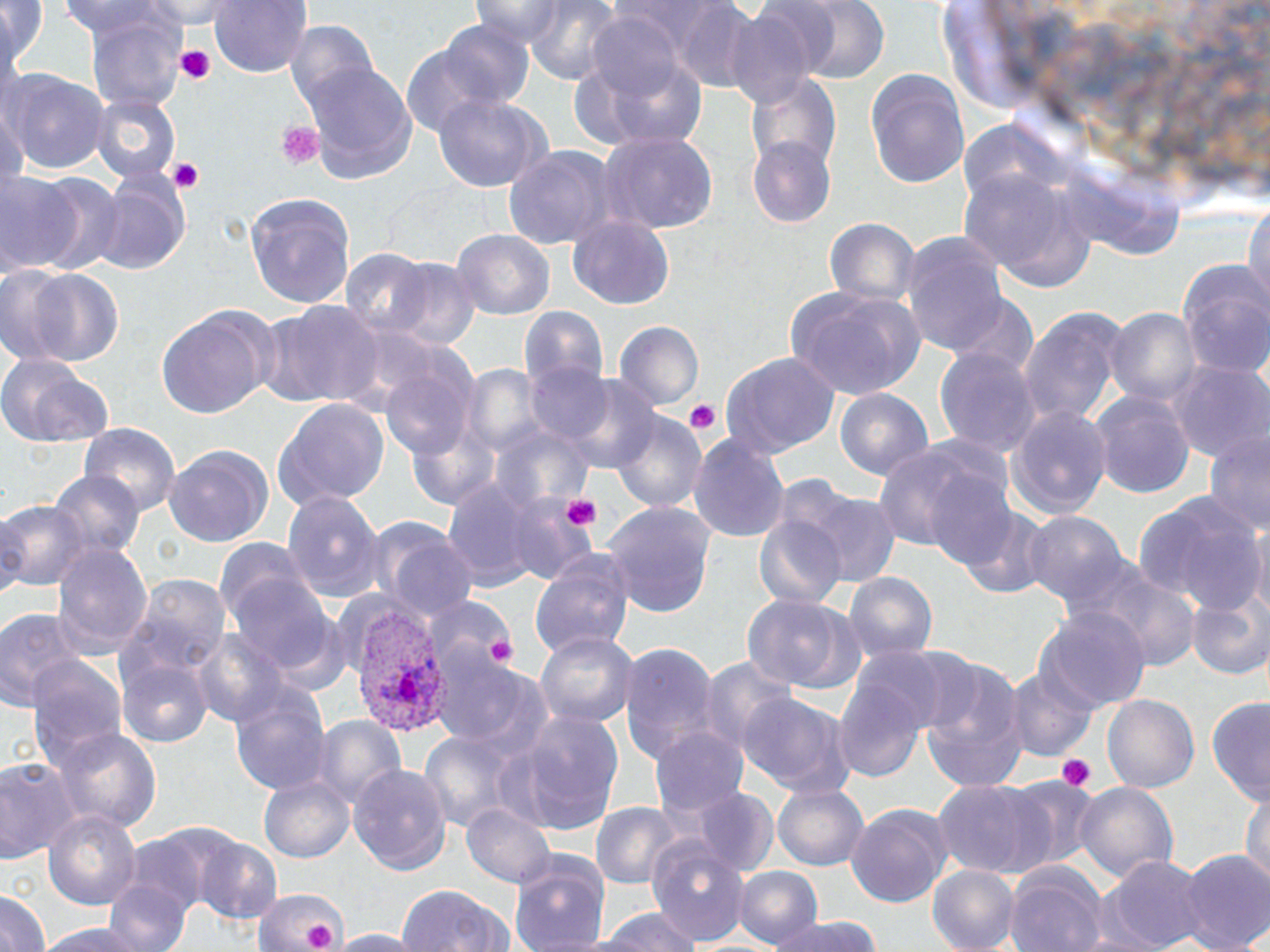 Approximate bounding boxes as named x1/y1/x2/y2 corners in pixels. Uninfected red blood cell locations: (x1=0, y1=0, x2=47, y2=87), (x1=144, y1=0, x2=250, y2=29), (x1=209, y1=0, x2=311, y2=80), (x1=469, y1=0, x2=575, y2=42), (x1=521, y1=0, x2=627, y2=86), (x1=789, y1=0, x2=890, y2=84), (x1=53, y1=2, x2=185, y2=42), (x1=664, y1=2, x2=762, y2=89), (x1=81, y1=7, x2=192, y2=116), (x1=721, y1=7, x2=821, y2=112), (x1=583, y1=10, x2=691, y2=104), (x1=432, y1=17, x2=536, y2=111), (x1=286, y1=22, x2=383, y2=123), (x1=400, y1=42, x2=504, y2=139), (x1=570, y1=47, x2=710, y2=158), (x1=299, y1=60, x2=417, y2=182), (x1=864, y1=67, x2=970, y2=189), (x1=4, y1=71, x2=109, y2=178), (x1=745, y1=71, x2=841, y2=174), (x1=92, y1=94, x2=180, y2=184), (x1=432, y1=94, x2=550, y2=193), (x1=599, y1=132, x2=717, y2=236), (x1=747, y1=137, x2=837, y2=229), (x1=502, y1=144, x2=622, y2=249), (x1=954, y1=167, x2=1094, y2=287), (x1=93, y1=170, x2=192, y2=274), (x1=24, y1=171, x2=122, y2=277), (x1=0, y1=175, x2=82, y2=272), (x1=246, y1=194, x2=355, y2=308), (x1=1243, y1=201, x2=1270, y2=320), (x1=568, y1=214, x2=676, y2=312), (x1=825, y1=218, x2=920, y2=309), (x1=451, y1=231, x2=554, y2=321), (x1=899, y1=234, x2=1012, y2=360), (x1=337, y1=248, x2=439, y2=343), (x1=1176, y1=258, x2=1270, y2=379), (x1=389, y1=262, x2=480, y2=354), (x1=19, y1=267, x2=124, y2=369), (x1=784, y1=286, x2=927, y2=399), (x1=946, y1=297, x2=1039, y2=382), (x1=254, y1=299, x2=381, y2=409), (x1=1017, y1=304, x2=1132, y2=429), (x1=157, y1=305, x2=273, y2=418), (x1=521, y1=306, x2=607, y2=392), (x1=1105, y1=308, x2=1200, y2=414), (x1=614, y1=321, x2=704, y2=410), (x1=934, y1=347, x2=1038, y2=456), (x1=722, y1=351, x2=840, y2=455), (x1=0, y1=354, x2=117, y2=450), (x1=383, y1=358, x2=476, y2=462), (x1=1170, y1=360, x2=1267, y2=461), (x1=524, y1=362, x2=616, y2=447), (x1=562, y1=376, x2=662, y2=477), (x1=833, y1=388, x2=934, y2=486), (x1=1090, y1=392, x2=1197, y2=499), (x1=274, y1=396, x2=391, y2=511), (x1=1006, y1=407, x2=1113, y2=519), (x1=610, y1=409, x2=705, y2=513), (x1=80, y1=422, x2=178, y2=513), (x1=689, y1=431, x2=790, y2=546), (x1=1203, y1=431, x2=1270, y2=539), (x1=875, y1=439, x2=1010, y2=561), (x1=162, y1=444, x2=272, y2=550), (x1=53, y1=471, x2=143, y2=564), (x1=927, y1=473, x2=1021, y2=570), (x1=440, y1=477, x2=552, y2=593), (x1=798, y1=488, x2=900, y2=587), (x1=282, y1=489, x2=385, y2=603), (x1=1135, y1=491, x2=1263, y2=616), (x1=503, y1=496, x2=597, y2=583), (x1=0, y1=499, x2=91, y2=599), (x1=603, y1=502, x2=715, y2=619), (x1=959, y1=507, x2=1057, y2=601), (x1=367, y1=512, x2=473, y2=621), (x1=1022, y1=512, x2=1129, y2=612), (x1=754, y1=513, x2=846, y2=611), (x1=1251, y1=518, x2=1269, y2=619), (x1=51, y1=539, x2=153, y2=659), (x1=531, y1=549, x2=637, y2=663), (x1=1066, y1=558, x2=1199, y2=670), (x1=844, y1=571, x2=938, y2=663), (x1=224, y1=573, x2=344, y2=679), (x1=120, y1=575, x2=230, y2=693), (x1=1187, y1=591, x2=1270, y2=680), (x1=426, y1=593, x2=518, y2=671), (x1=740, y1=594, x2=852, y2=695), (x1=0, y1=606, x2=83, y2=714), (x1=1040, y1=607, x2=1150, y2=711), (x1=536, y1=628, x2=638, y2=732), (x1=193, y1=629, x2=290, y2=729), (x1=618, y1=643, x2=720, y2=763), (x1=890, y1=646, x2=984, y2=735), (x1=700, y1=655, x2=796, y2=755), (x1=119, y1=657, x2=210, y2=746), (x1=26, y1=658, x2=126, y2=772), (x1=437, y1=661, x2=555, y2=758), (x1=921, y1=662, x2=1028, y2=790), (x1=1006, y1=662, x2=1099, y2=760), (x1=832, y1=672, x2=930, y2=785), (x1=230, y1=680, x2=331, y2=797), (x1=738, y1=692, x2=856, y2=796), (x1=1101, y1=695, x2=1199, y2=794), (x1=1208, y1=701, x2=1270, y2=805), (x1=507, y1=709, x2=626, y2=836), (x1=311, y1=716, x2=408, y2=811), (x1=55, y1=723, x2=162, y2=834), (x1=650, y1=725, x2=751, y2=822), (x1=417, y1=730, x2=521, y2=835), (x1=0, y1=758, x2=78, y2=866), (x1=348, y1=763, x2=452, y2=874), (x1=260, y1=773, x2=354, y2=864), (x1=1005, y1=775, x2=1105, y2=869), (x1=932, y1=780, x2=1057, y2=880), (x1=773, y1=781, x2=870, y2=870), (x1=1074, y1=781, x2=1177, y2=883), (x1=694, y1=790, x2=779, y2=880), (x1=1241, y1=791, x2=1270, y2=889), (x1=592, y1=801, x2=681, y2=893), (x1=462, y1=802, x2=558, y2=889), (x1=845, y1=804, x2=952, y2=907), (x1=43, y1=807, x2=143, y2=911), (x1=193, y1=838, x2=283, y2=925), (x1=648, y1=838, x2=753, y2=943), (x1=1181, y1=849, x2=1270, y2=952), (x1=510, y1=850, x2=612, y2=952), (x1=1105, y1=856, x2=1209, y2=950), (x1=1005, y1=864, x2=1108, y2=952), (x1=733, y1=866, x2=822, y2=948), (x1=927, y1=866, x2=1019, y2=951), (x1=105, y1=879, x2=195, y2=952), (x1=395, y1=884, x2=515, y2=952), (x1=253, y1=886, x2=347, y2=952), (x1=0, y1=892, x2=52, y2=952), (x1=590, y1=906, x2=703, y2=952), (x1=772, y1=915, x2=884, y2=952), (x1=35, y1=918, x2=166, y2=952), (x1=323, y1=930, x2=423, y2=951). Plasmodium vivax-infected red blood cell locations: (x1=342, y1=608, x2=449, y2=735). Platelet locations: (x1=175, y1=45, x2=217, y2=87), (x1=276, y1=120, x2=325, y2=170), (x1=167, y1=158, x2=205, y2=192), (x1=683, y1=399, x2=721, y2=435), (x1=559, y1=494, x2=603, y2=531), (x1=487, y1=634, x2=515, y2=666), (x1=1056, y1=756, x2=1095, y2=790), (x1=303, y1=920, x2=334, y2=948). Slide-level diagnosis: Plasmodium vivax. Thin blood film. Optical microscopy. One field of a larger specimen. Image is 1270×952 pixels. May-Grünwald-Giemsa stain. 1000x magnification.